Classify this cell by malaria status.
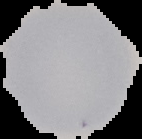

Uninfected.

image type = segmented cell region on a black background
image size = 142×139 pixels
preparation = thin blood smear